Identify the cell.
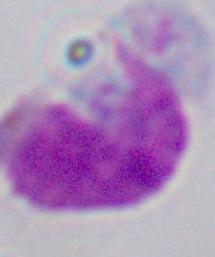
This is a leukocyte.

modality = photomicrograph
magnification = 1000x